Assess the morphology of the erythrocytes.
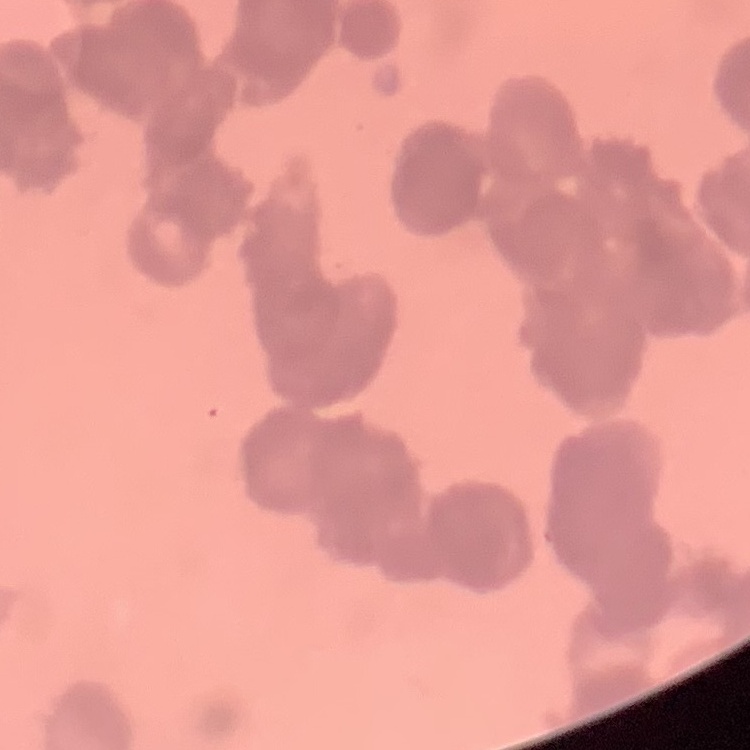

Rouleaux formation.

{
  "image_type": "one tile cut from a larger photomicrograph",
  "preparation": "thin peripheral smear",
  "stain": "Field's or Giemsa"
}